Locate every Plasmodium falciparum-infected red blood cell.
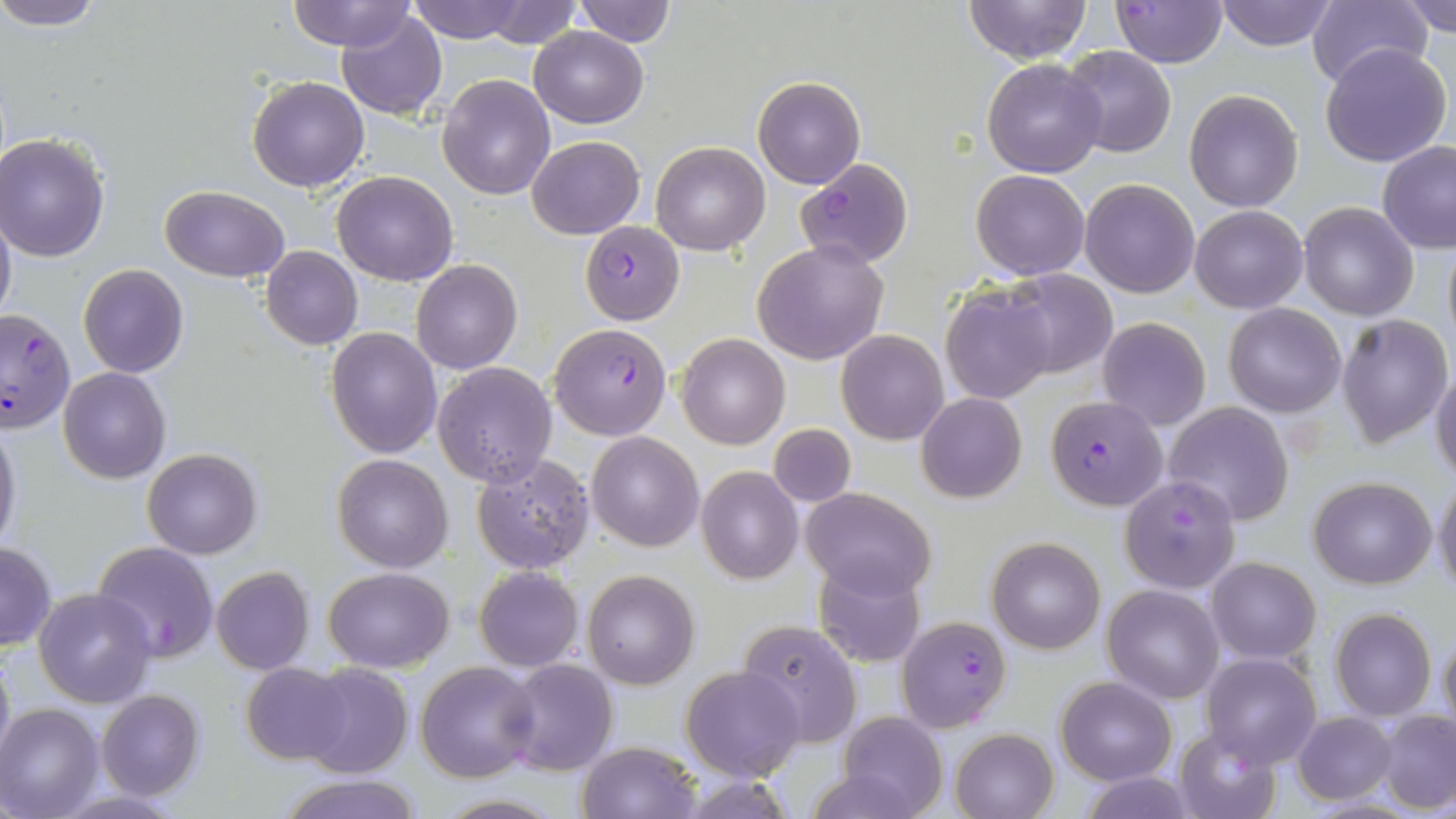

Approximate bounding boxes as [x1, y1, x2, y2] in pixels.
Plasmodium falciparum-infected red blood cells: [1112, 1, 1228, 68], [794, 157, 913, 268], [580, 220, 684, 325], [0, 307, 76, 431], [550, 321, 673, 440], [1047, 394, 1165, 511], [1120, 473, 1241, 594], [92, 541, 218, 662], [895, 615, 1013, 732].

slide-level diagnosis = Plasmodium falciparum
field of view = single
preparation = thin blood smear
image size = 1456×819 pixels
stain = May-Grünwald-Giemsa
uninfected red blood cell locations = approximate bounding boxes as [x1, y1, x2, y2] in pixels: [2, 0, 105, 29], [286, 0, 418, 52], [409, 0, 527, 43], [961, 0, 1094, 66], [1214, 0, 1339, 50], [1305, 0, 1432, 89], [1399, 0, 1456, 36], [476, 1, 582, 48], [570, 1, 676, 46], [336, 8, 447, 119], [530, 25, 648, 127], [1320, 41, 1453, 167], [1061, 46, 1176, 159], [983, 57, 1109, 179], [246, 75, 369, 191], [437, 75, 555, 200], [752, 76, 865, 189], [1184, 90, 1304, 211], [1, 133, 113, 261], [527, 135, 645, 238], [652, 140, 771, 255], [1377, 141, 1456, 253], [971, 169, 1090, 279], [333, 171, 457, 286], [1079, 178, 1199, 298], [160, 184, 290, 282], [1297, 202, 1419, 320], [1190, 205, 1306, 312], [0, 208, 16, 327], [1442, 237, 1456, 354], [753, 239, 887, 365], [261, 247, 363, 349], [411, 259, 523, 374], [78, 264, 188, 378], [1001, 269, 1118, 380], [940, 285, 1056, 404], [1222, 302, 1346, 417], [1336, 313, 1453, 447], [1097, 317, 1211, 430], [325, 328, 443, 458], [836, 330, 949, 445], [676, 332, 789, 449], [432, 361, 558, 488], [1430, 363, 1456, 482], [58, 367, 170, 483], [917, 393, 1027, 504], [1163, 402, 1295, 525], [0, 415, 21, 557], [768, 422, 855, 508], [587, 432, 703, 550], [142, 447, 262, 560], [472, 452, 597, 574], [331, 453, 453, 571], [697, 466, 803, 583], [1309, 475, 1437, 589], [1433, 480, 1456, 595], [800, 485, 936, 600], [987, 535, 1106, 655], [0, 542, 54, 651], [1205, 555, 1321, 663], [812, 560, 927, 668], [474, 565, 585, 671], [211, 567, 315, 675], [323, 567, 454, 673], [583, 570, 700, 690], [1101, 584, 1224, 703], [33, 587, 157, 708], [1328, 609, 1437, 721], [736, 620, 864, 749], [1437, 629, 1456, 739], [0, 642, 14, 771], [1201, 653, 1321, 768], [499, 658, 617, 776], [415, 661, 539, 782], [240, 663, 355, 765], [300, 663, 413, 779], [681, 664, 805, 781], [1056, 677, 1175, 784], [96, 690, 204, 801], [0, 703, 104, 818], [1378, 711, 1456, 813], [838, 712, 948, 819], [1293, 712, 1396, 804], [1172, 727, 1281, 819], [951, 729, 1057, 818], [577, 740, 703, 819], [1082, 773, 1198, 817], [277, 774, 423, 819], [431, 794, 566, 818]
magnification = 1000x
modality = light microscopy